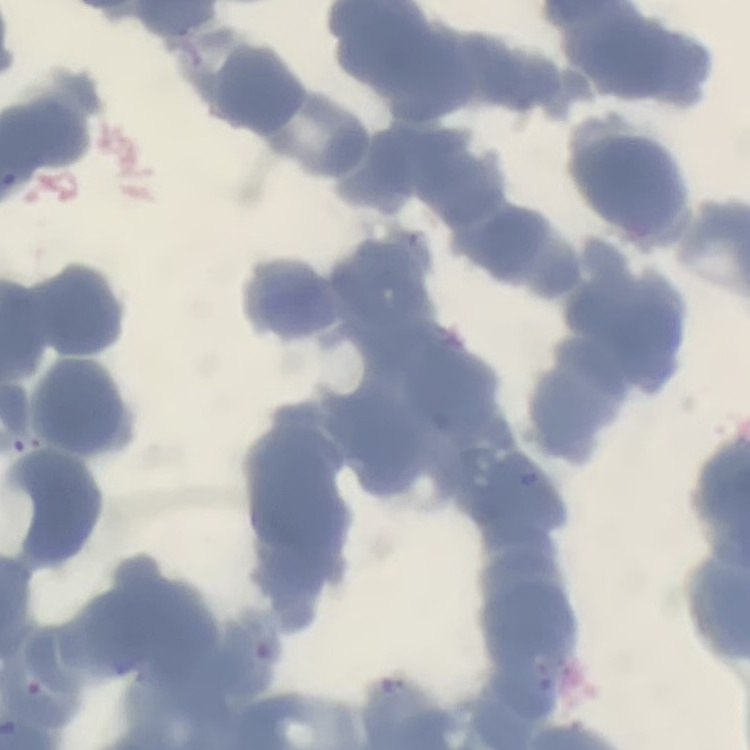 The erythrocytes exhibit rouleaux formation. Stained with either Field's or Giemsa. Thin peripheral smear. One tile cut from a larger photomicrograph.